Classify this cell by malaria status.
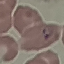

It is parasitized.

Thin blood film. Cell patch, automatically extracted from a larger field of view and resized to 64 × 64 pixels. Photographed with a smartphone camera at the microscope eyepiece. Giemsa-stained preparation.